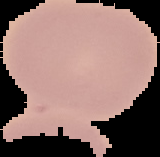
Summary:
  - Preparation: thin blood film
  - Image size: 160×157 pixels
  - Image type: segmented cell region with the area outside set to black
  - Malaria status: uninfected